Name the parasite shown.
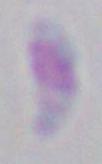
This is Toxoplasma gondii.

Captured at 1000x magnification. Photomicrograph.